Locate every Plasmodium parasite.
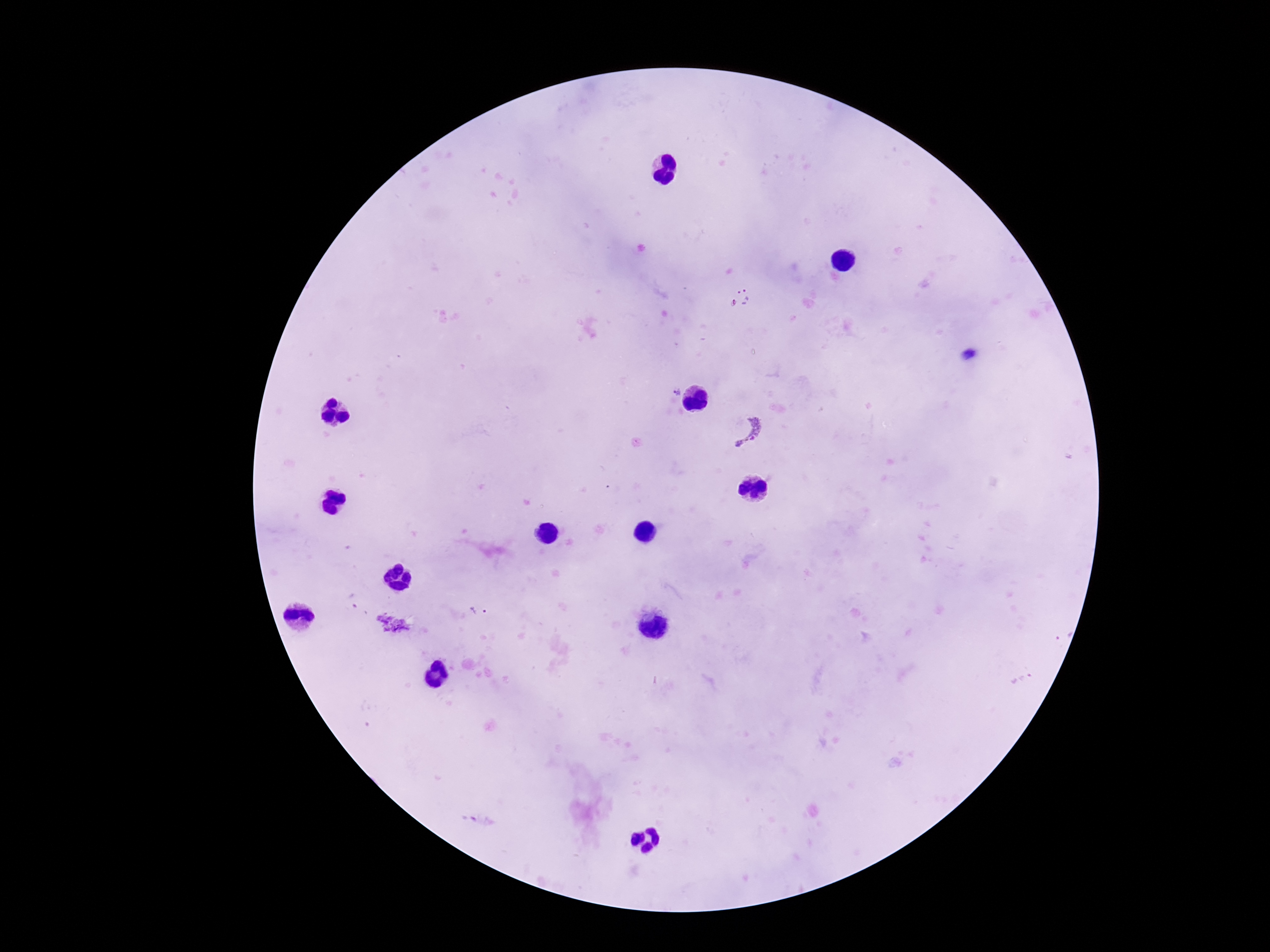
Approximate centers as [x, y] in pixels.
Plasmodium parasites: [741, 298], [673, 392], [747, 430].

magnification = 100x
stain = Giemsa
capture = smartphone camera through the microscope eyepiece
patient malaria status = infected
preparation = thick blood smear
image size = 1270×952 pixels
field of view = one from this slide